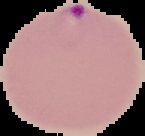 Cell region segmented out of the field of view; the surrounding area is masked to black. Image is 145×136 pixels. Malaria status: parasitized. From a thin blood smear.